Name the parasite shown.
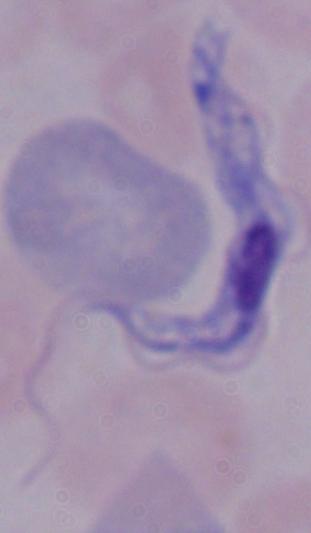
A trypanosome.

Captured at 1000x magnification. Photomicrograph.